Point out each malaria parasite.
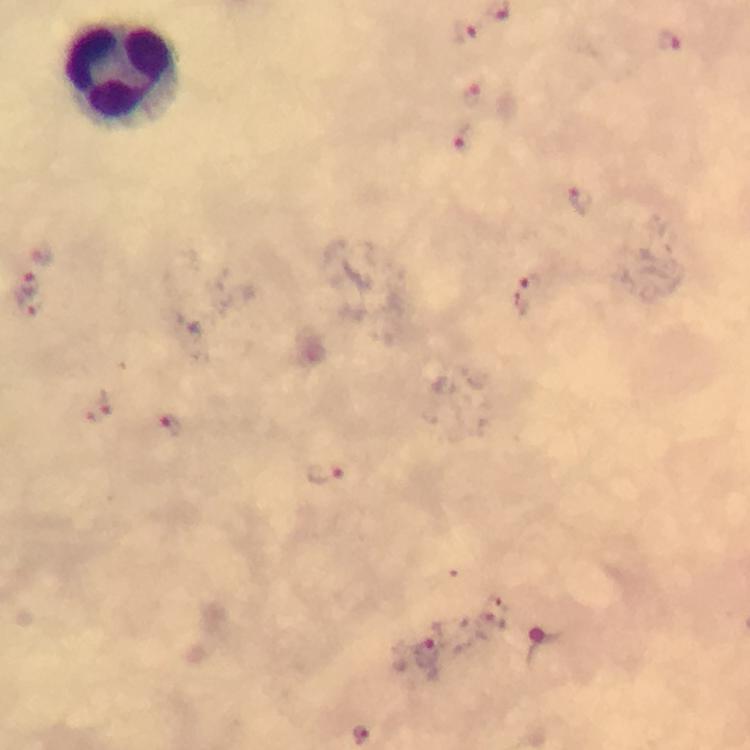

Approximate centers as (x, y) in pixels.
Malaria parasites: (466, 32), (669, 41), (476, 96), (466, 138), (581, 199), (41, 254), (30, 285), (526, 293), (26, 305), (98, 409), (169, 424), (322, 473), (488, 625), (425, 653).

Leukocyte locations: (124, 75). Photographed through the microscope with a smartphone camera. A crop from one field of view. 100x magnification. Giemsa-stained preparation. Image is 750×750 pixels. Immersion oil applied. From a diagnostic examination for malaria. Thick blood film.